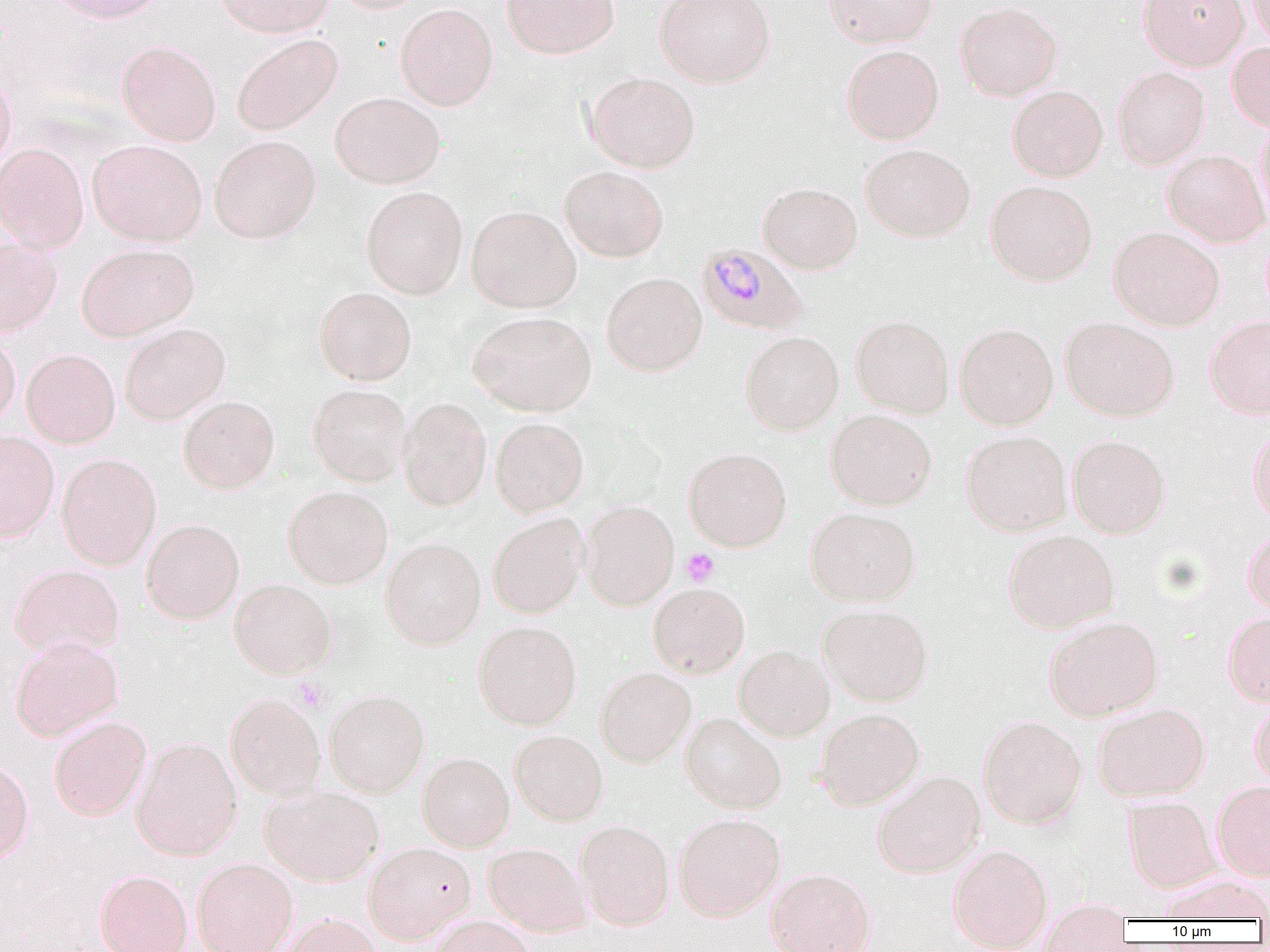
slide_level_diagnosis: Plasmodium malariae
magnification: 1000x
platelet_locations: 'approximate bounding boxes as (x1,y1)-(x2,y2) corner pairs in pixels: (681,548)-(719,586), (293,677)-(330,712)'
plasmodium_malariae_infected_red_blood_cell_locations: 'approximate bounding boxes as (x1,y1)-(x2,y2) corner pairs in pixels: (696,243)-(808,335)'
image_size: 1270×952 pixels
field_of_view: one of a larger specimen
modality: optical microscopy
preparation: thin blood film
uninfected_red_blood_cell_locations: 'approximate bounding boxes as (x1,y1)-(x2,y2) corner pairs in pixels: (49,0)-(170,23), (214,0)-(335,37), (331,0)-(428,14), (500,0)-(620,60), (655,0)-(776,88), (822,0)-(939,48), (1138,0)-(1250,70), (1248,0)-(1270,51), (955,1)-(1063,101), (395,3)-(499,110), (232,34)-(342,136), (116,40)-(222,147), (1227,42)-(1270,131), (841,44)-(944,145), (1113,66)-(1211,169), (0,69)-(17,175), (584,71)-(701,173), (1007,85)-(1108,182), (330,92)-(446,188), (1254,115)-(1270,228), (209,134)-(322,243), (87,139)-(208,246), (0,142)-(89,253), (860,144)-(976,242), (1163,149)-(1270,248), (559,166)-(669,262), (985,180)-(1098,286), (758,182)-(862,274), (361,186)-(468,298), (466,205)-(581,313), (1109,226)-(1225,331), (0,237)-(62,337), (76,243)-(199,341), (601,272)-(707,376), (314,287)-(417,385), (468,310)-(596,416), (850,315)-(955,419), (1204,315)-(1270,419), (1060,317)-(1180,421), (955,322)-(1058,430), (119,323)-(230,424), (740,331)-(844,435), (0,334)-(21,428), (21,348)-(120,448), (307,383)-(413,487), (178,395)-(280,494), (398,397)-(492,510), (825,409)-(937,510), (490,417)-(589,516), (1248,425)-(1270,526), (0,430)-(60,542), (961,430)-(1072,536), (1067,434)-(1170,538), (683,447)-(792,552), (56,453)-(162,569), (283,486)-(393,589), (579,500)-(679,611), (805,507)-(921,606), (487,513)-(588,618), (141,518)-(245,624), (1002,529)-(1120,633), (1242,530)-(1270,618), (380,536)-(485,650), (8,564)-(125,657), (229,578)-(337,679), (647,582)-(750,678), (818,603)-(933,706), (1222,612)-(1270,706), (1044,616)-(1164,721), (473,621)-(582,729), (10,636)-(124,741), (734,644)-(835,741), (595,667)-(696,767), (324,689)-(430,797), (225,692)-(326,800), (1249,699)-(1270,790), (1093,702)-(1210,802), (815,708)-(925,810), (680,712)-(787,813), (978,715)-(1086,829), (49,716)-(151,821), (509,729)-(608,826), (131,737)-(243,860), (418,752)-(515,851), (0,759)-(34,864), (873,771)-(986,878), (1211,781)-(1270,880), (260,785)-(384,886), (1123,795)-(1220,892), (673,812)-(786,921), (574,819)-(675,930), (363,842)-(476,944), (483,842)-(591,936), (948,843)-(1053,951), (193,857)-(298,952), (766,868)-(876,952), (95,869)-(193,952), (1159,876)-(1270,922), (1038,908)-(1133,951), (276,912)-(384,952), (429,914)-(538,952)'